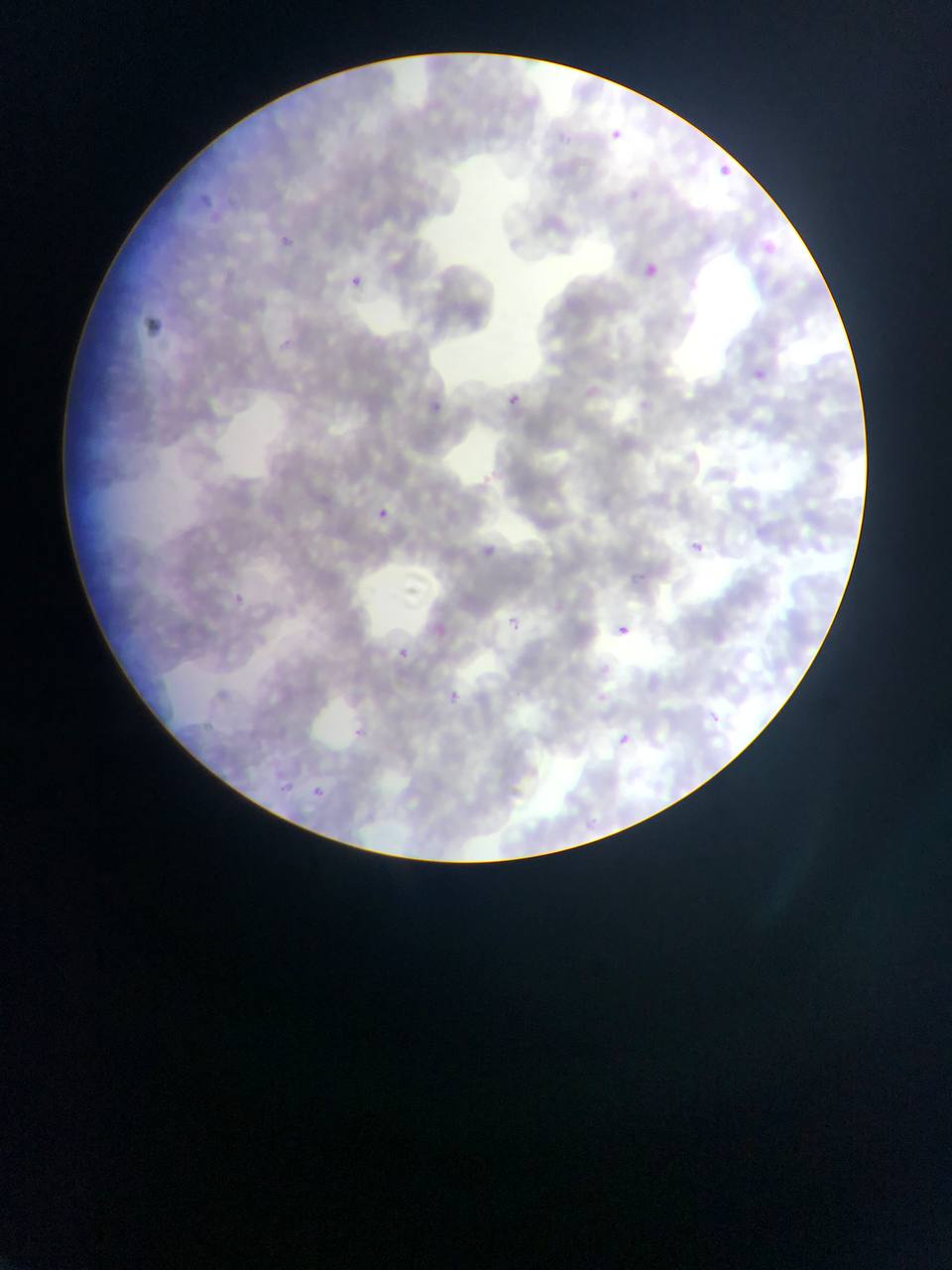
country: Ghana
capture: mobile-phone photograph through a microscope
image_size: 952×1270 pixels
field_of_view: single
plasmodium_parasite_locations: 'approximate bounding boxes as {left, top, right, bottom} in pixels: {591, 112, 625, 153}, {719, 165, 753, 188}, {280, 235, 292, 246}, {764, 236, 794, 250}, {632, 266, 672, 299}, {349, 275, 363, 287}, {749, 359, 768, 373}, {507, 393, 521, 406}, {430, 399, 442, 412}, {374, 507, 402, 531}, {487, 537, 508, 559}, {690, 540, 704, 553}, {233, 592, 245, 605}, {505, 605, 520, 626}, {617, 625, 627, 634}, {385, 639, 414, 673}, {443, 687, 465, 701}, {346, 720, 375, 741}, {609, 734, 645, 755}, {316, 782, 340, 804}'
preparation: thin blood smear